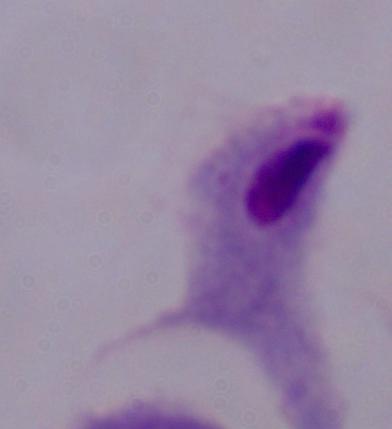
Captured at 1000x magnification. A trichomonad is shown. Photomicrograph.